Comment on the morphology of the red blood cells.
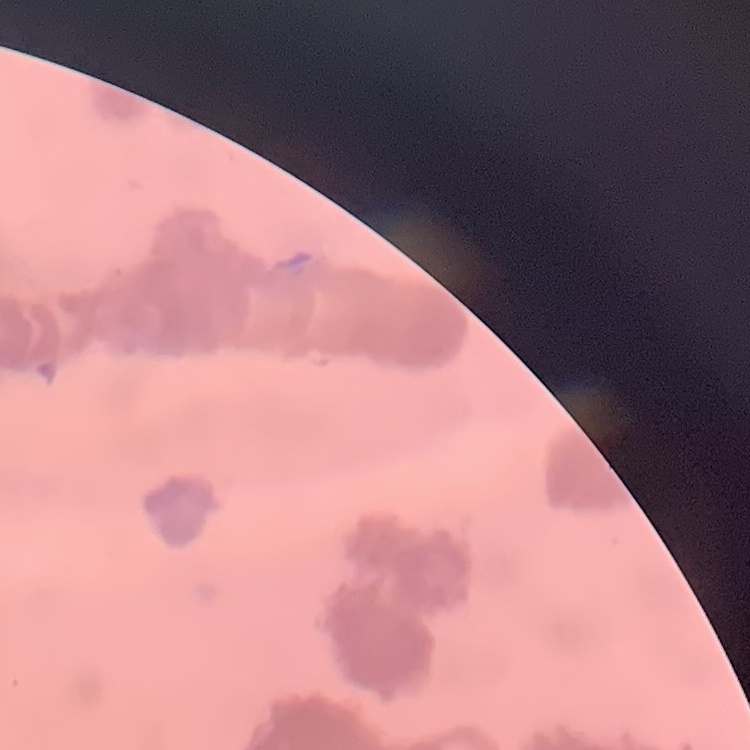
Rouleaux formation.

stain = Field's or Giemsa
image type = one tile cut from a larger photomicrograph
preparation = thin blood film